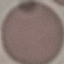

malaria_status: uninfected
capture: smartphone through the microscope eyepiece
image_type: automatically extracted cell patch, resized to 64 × 64 pixels
preparation: thin blood smear
stain: Giemsa